Assess the morphology of the red blood cells.
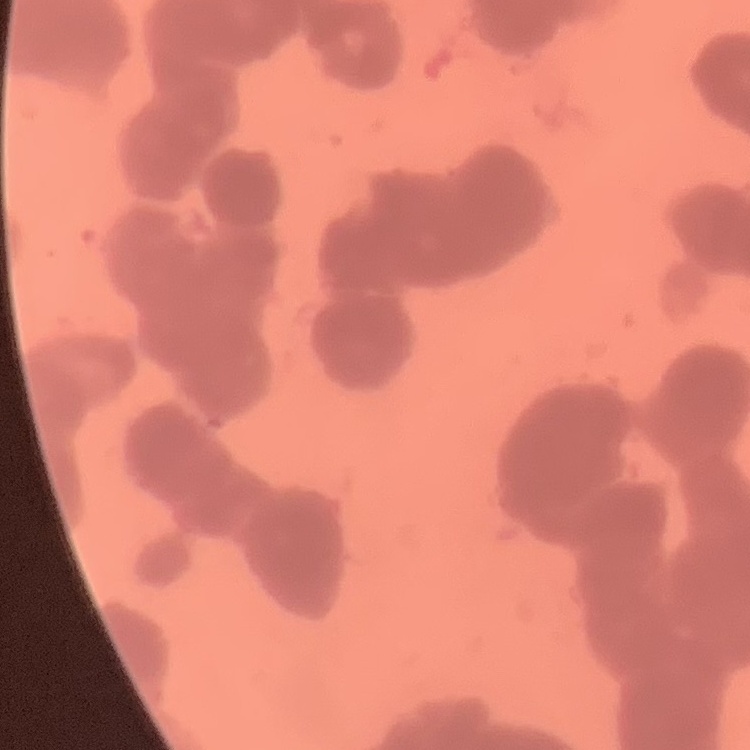
Rouleaux formation.

{
  "stain": "Field's or Giemsa",
  "preparation": "thin blood film",
  "image_type": "one tile cut from a larger photomicrograph"
}